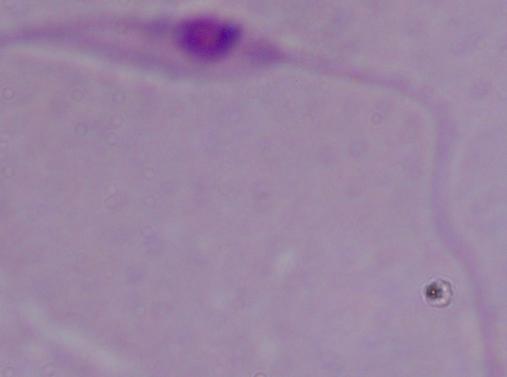

Summary:
  - Modality: photomicrograph
  - Identification: Leishmania
  - Magnification: 1000x